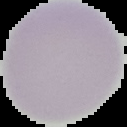

Summary:
  - Malaria status: uninfected
  - Image type: segmented cell region with the area outside set to black
  - Preparation: thin blood smear
  - Image size: 127×127 pixels